Identify the parasite.
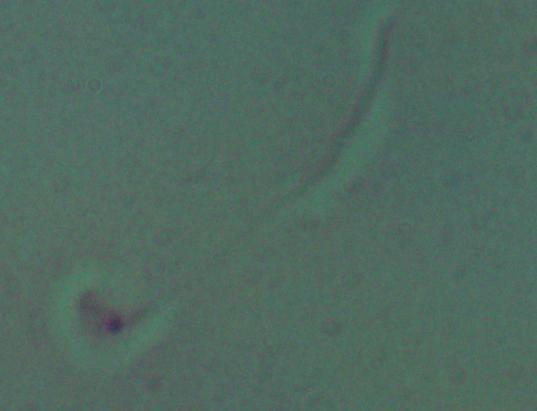

Leishmania.

magnification = 1000x
modality = micrograph